Identify the parasite.
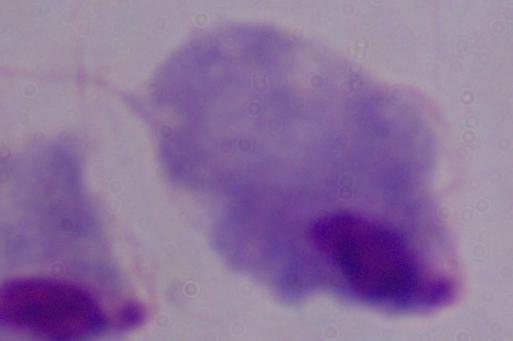
A trichomonad.

Photomicrograph. 1000x magnification.